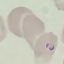
Summary:
  - Result: malaria parasites identified
  - Image type: automatically extracted cell patch, resized to 64 × 64 pixels
  - Stain: Giemsa
  - Capture: smartphone camera at the microscope eyepiece
  - Preparation: thin smear